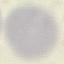
malaria status = uninfected
capture = smartphone through the microscope eyepiece
stain = Giemsa
preparation = thin blood film
image type = automatically extracted cell patch, resized to 64 × 64 pixels